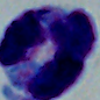

Summary:
  - Modality: micrograph
  - Magnification: 1000x
  - Identification: leukocyte